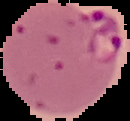

preparation = thin blood smear
result = Plasmodium parasites detected
image type = segmented cell region with the area outside set to black
image size = 130×121 pixels